Point out every Plasmodium parasite and every leukocyte.
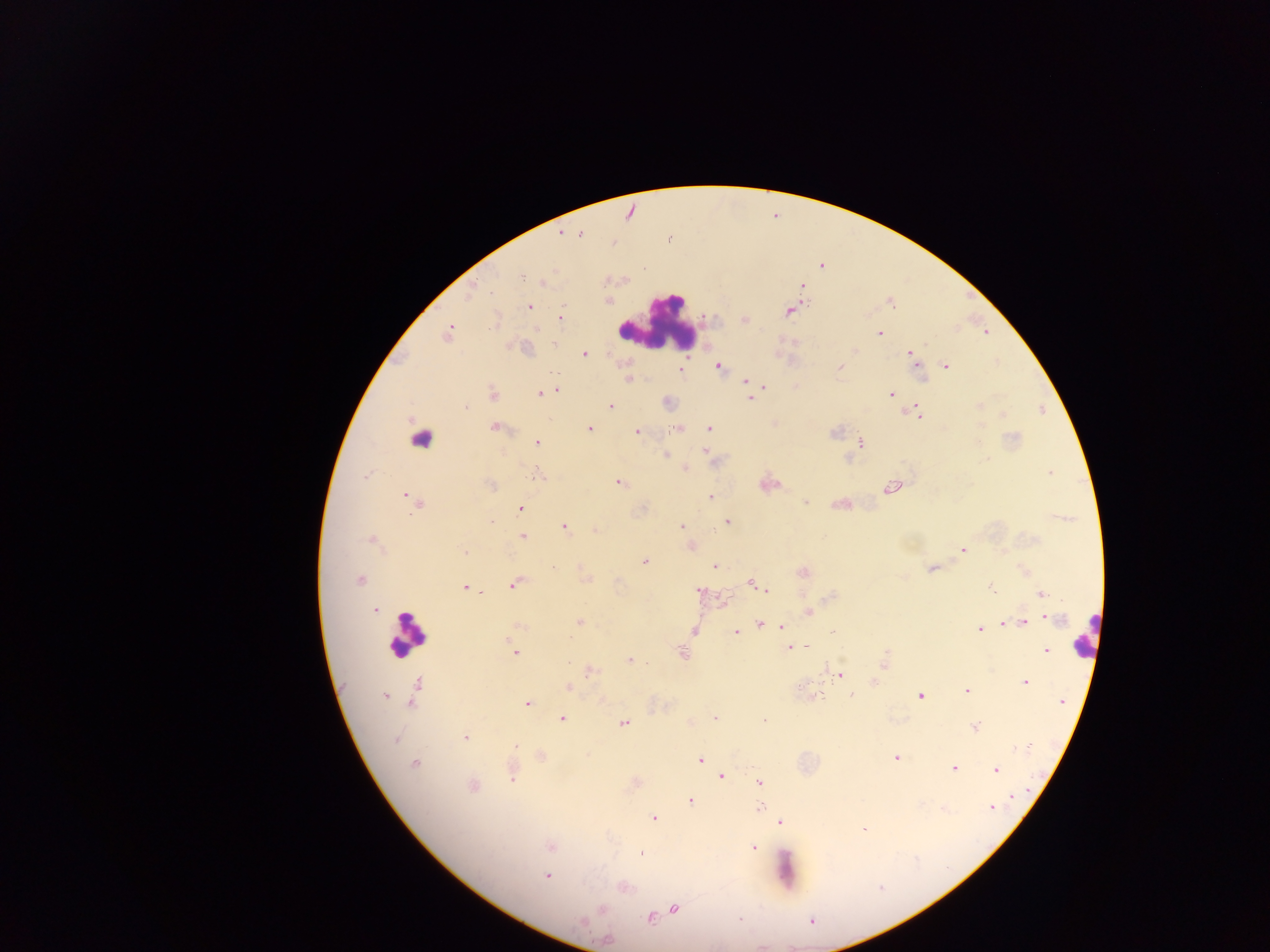

Approximate centers as {x, y} in pixels.
Plasmodium parasites: {630, 211}, {560, 233}, {580, 233}, {821, 266}, {523, 276}, {543, 282}, {802, 286}, {470, 289}, {606, 300}, {890, 301}, {528, 306}, {789, 310}, {561, 319}, {744, 319}, {985, 330}, {448, 333}, {879, 333}, {582, 353}, {909, 353}, {719, 366}, {945, 366}, {839, 368}, {679, 369}, {921, 377}, {629, 378}, {745, 382}, {763, 386}, {796, 387}, {555, 389}, {541, 393}, {890, 393}, {492, 394}, {750, 398}, {667, 401}, {979, 405}, {609, 406}, {465, 407}, {915, 413}, {1002, 413}, {774, 424}, {495, 427}, {589, 428}, {676, 428}, {709, 428}, {638, 431}, {536, 442}, {860, 442}, {706, 450}, {665, 455}, {684, 467}, {1050, 472}, {538, 476}, {618, 482}, {768, 483}, {491, 485}, {890, 488}, {407, 497}, {710, 497}, {414, 501}, {805, 502}, {840, 504}, {520, 509}, {726, 521}, {563, 526}, {681, 527}, {595, 529}, {522, 536}, {372, 539}, {692, 546}, {962, 549}, {464, 551}, {645, 560}, {715, 565}, {932, 567}, {1023, 569}, {803, 572}, {585, 578}, {359, 579}, {515, 583}, {751, 583}, {465, 588}, {991, 588}, {700, 591}, {767, 591}, {1041, 594}, {719, 598}, {376, 609}, {809, 612}, {1044, 615}, {580, 622}, {1004, 622}, {1022, 623}, {759, 624}, {518, 626}, {782, 626}, {978, 629}, {735, 630}, {832, 630}, {693, 631}, {789, 646}, {1045, 650}, {515, 652}, {683, 654}, {629, 660}, {883, 661}, {587, 671}, {839, 675}, {873, 681}, {1024, 681}, {416, 683}, {568, 687}, {966, 691}, {384, 693}, {852, 694}, {814, 696}, {919, 696}, {1060, 701}, {411, 703}, {527, 703}, {714, 717}, {561, 718}, {763, 721}, {689, 722}, {623, 724}, {973, 726}, {465, 737}, {540, 756}, {896, 757}, {700, 759}, {414, 764}, {954, 768}, {995, 770}, {512, 774}, {721, 775}, {635, 782}, {759, 782}, {472, 786}, {1011, 796}, {690, 800}, {759, 807}, {943, 807}, {991, 807}, {653, 818}, {780, 821}, {864, 828}, {550, 846}, {753, 847}, {640, 852}, {547, 875}, {622, 886}, {673, 907}, {649, 917}, {606, 939}.
Leukocytes: {659, 324}, {423, 446}, {408, 634}, {1085, 638}, {785, 871}.

Mobile-phone photograph taken through the microscope. Image is 1270×952 pixels. Sample from Ghana. Thick blood smear. Single field of view.